Report the malaria status of this cell.
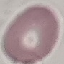
It is uninfected.

Summary:
  - Preparation: thin blood smear
  - Image type: automatically extracted cell patch, resized to 64 × 64 pixels
  - Capture: smartphone through the microscope eyepiece
  - Stain: Giemsa